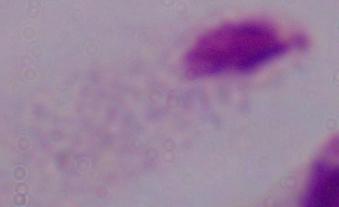

{
  "modality": "photomicrograph",
  "identification": "trichomonad",
  "magnification": "1000x"
}